Outline each Plasmodium falciparum-infected red blood cell.
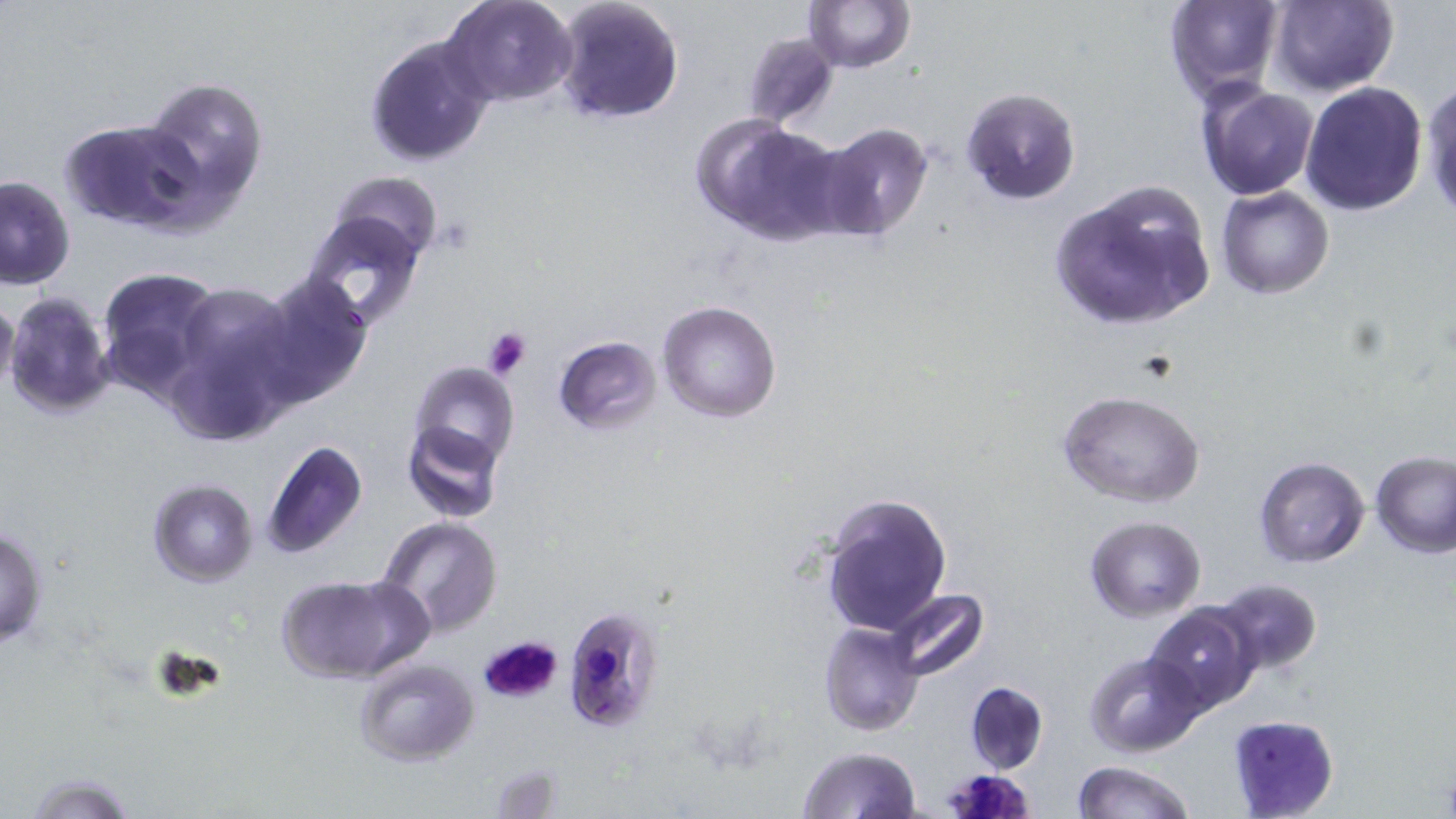

Approximate bounding boxes as [x1, y1, x2, y2] in pixels.
Plasmodium falciparum-infected red blood cells: [561, 605, 665, 734], [945, 766, 1035, 819].

{
  "slide_level_diagnosis": "Plasmodium falciparum",
  "stain": "May-Grünwald-Giemsa",
  "image_size": "1456×819 pixels",
  "preparation": "thin blood film",
  "field_of_view": "one of a larger specimen",
  "platelet_locations": "approximate bounding boxes as [x1, y1, x2, y2] in pixels: [481, 325, 534, 380], [477, 634, 565, 708]",
  "modality": "light microscopy",
  "uninfected_red_blood_cell_locations": "approximate bounding boxes as [x1, y1, x2, y2] in pixels: [444, 0, 578, 107], [551, 0, 685, 125], [803, 0, 915, 73], [1164, 0, 1285, 101], [1269, 0, 1398, 97], [740, 31, 838, 131], [362, 34, 496, 169], [133, 74, 270, 227], [1419, 79, 1456, 222], [1300, 81, 1429, 215], [1195, 82, 1319, 200], [959, 87, 1081, 206], [693, 116, 846, 244], [58, 118, 199, 230], [811, 123, 937, 244], [329, 170, 443, 267], [0, 174, 75, 289], [1048, 178, 1217, 337], [1216, 187, 1334, 298], [300, 211, 428, 334], [95, 267, 222, 396], [251, 273, 372, 407], [168, 282, 298, 430], [4, 290, 118, 419], [0, 291, 19, 397], [657, 300, 783, 423], [553, 335, 661, 434], [407, 361, 519, 472], [1057, 389, 1206, 508], [400, 419, 504, 525], [260, 439, 367, 563], [1371, 453, 1456, 558], [1254, 458, 1370, 567], [148, 479, 258, 587], [819, 492, 952, 634], [378, 516, 503, 637], [1085, 516, 1207, 622], [0, 526, 49, 649], [275, 573, 431, 684], [1209, 579, 1323, 676], [879, 588, 991, 682], [1146, 604, 1263, 715], [820, 622, 923, 735], [1084, 651, 1206, 757], [354, 657, 478, 766], [964, 680, 1050, 775], [1226, 715, 1339, 817], [796, 746, 922, 819], [1071, 760, 1197, 819], [19, 770, 141, 819]",
  "magnification": "1000x"
}